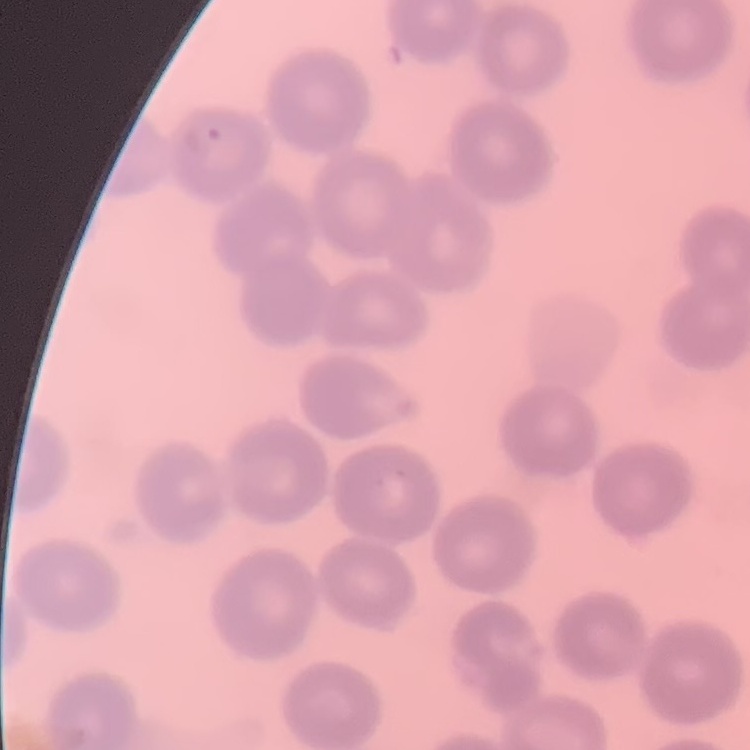
erythrocyte morphology = no rouleaux formation
preparation = thin blood film
image type = one tile cut from a larger photomicrograph
stain = Field's or Giemsa